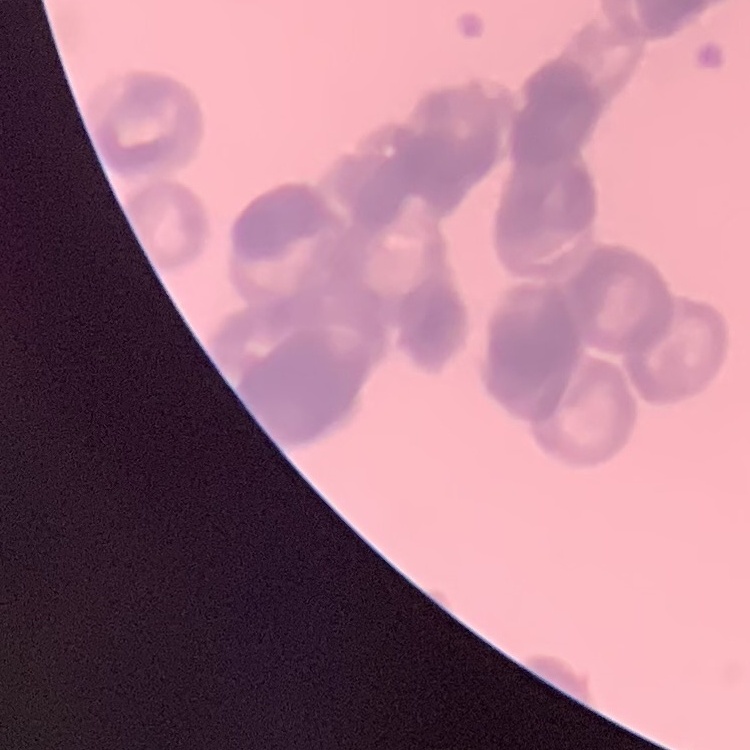
erythrocyte morphology = rouleaux formation
image type = square crop of a larger photomicrograph
preparation = thin blood smear
stain = Field's or Giemsa